Locate platelets.
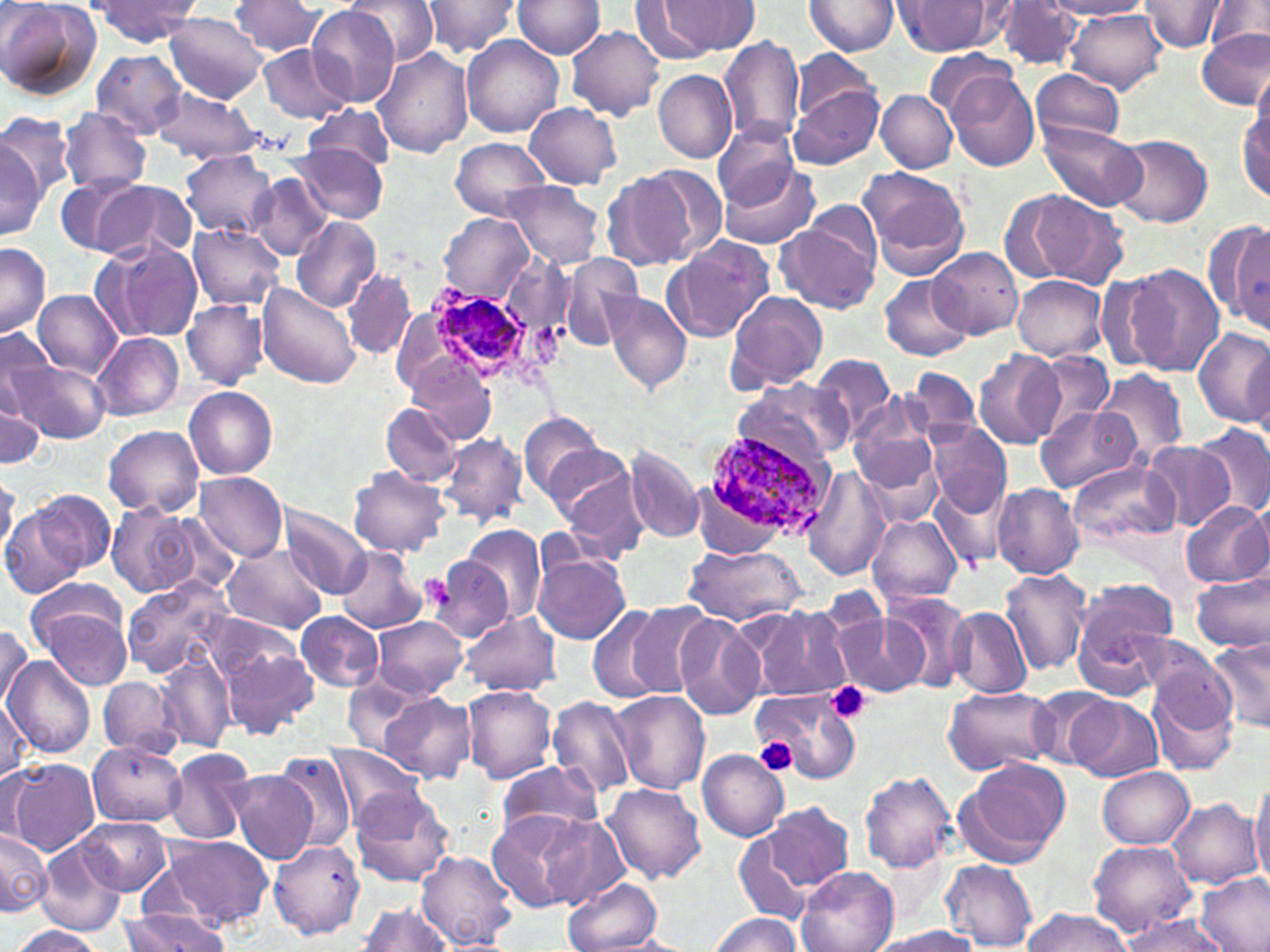
Approximate bounding boxes as named x1/y1/x2/y2 corners in pixels.
Platelets: (x1=826, y1=681, x2=872, y2=724), (x1=750, y1=737, x2=799, y2=777).

slide-level diagnosis = Plasmodium ovale
modality = optical microscopy
magnification = 1000x
field of view = single
preparation = thin blood smear
image size = 1270×952 pixels
uninfected red blood cell locations = approximate bounding boxes as named x1/y1/x2/y2 corners in pixels: (x1=346, y1=0, x2=438, y2=65), (x1=511, y1=0, x2=605, y2=59), (x1=1204, y1=0, x2=1268, y2=55), (x1=0, y1=1, x2=100, y2=102), (x1=231, y1=1, x2=323, y2=56), (x1=420, y1=1, x2=521, y2=59), (x1=668, y1=1, x2=761, y2=55), (x1=803, y1=1, x2=899, y2=57), (x1=999, y1=1, x2=1083, y2=71), (x1=1047, y1=1, x2=1152, y2=19), (x1=89, y1=2, x2=199, y2=47), (x1=629, y1=2, x2=721, y2=63), (x1=895, y1=2, x2=999, y2=57), (x1=1138, y1=2, x2=1224, y2=53), (x1=307, y1=6, x2=400, y2=107), (x1=1066, y1=8, x2=1169, y2=92), (x1=165, y1=13, x2=266, y2=103), (x1=564, y1=25, x2=663, y2=120), (x1=1197, y1=27, x2=1270, y2=110), (x1=718, y1=34, x2=806, y2=146), (x1=461, y1=35, x2=564, y2=138), (x1=258, y1=44, x2=352, y2=121), (x1=373, y1=48, x2=474, y2=158), (x1=793, y1=48, x2=879, y2=125), (x1=926, y1=48, x2=1018, y2=123), (x1=90, y1=49, x2=189, y2=139), (x1=1032, y1=69, x2=1126, y2=148), (x1=1248, y1=69, x2=1270, y2=164), (x1=653, y1=70, x2=737, y2=164), (x1=946, y1=71, x2=1040, y2=172), (x1=789, y1=86, x2=882, y2=168), (x1=151, y1=88, x2=267, y2=165), (x1=875, y1=90, x2=957, y2=173), (x1=525, y1=102, x2=621, y2=189), (x1=303, y1=103, x2=395, y2=171), (x1=1237, y1=106, x2=1269, y2=201), (x1=57, y1=109, x2=151, y2=194), (x1=0, y1=113, x2=77, y2=208), (x1=1038, y1=121, x2=1144, y2=212), (x1=713, y1=122, x2=801, y2=209), (x1=0, y1=133, x2=46, y2=237), (x1=1111, y1=134, x2=1214, y2=228), (x1=450, y1=138, x2=550, y2=221), (x1=294, y1=145, x2=387, y2=223), (x1=179, y1=150, x2=279, y2=240), (x1=718, y1=159, x2=820, y2=250), (x1=633, y1=166, x2=724, y2=264), (x1=858, y1=166, x2=970, y2=277), (x1=603, y1=169, x2=691, y2=271), (x1=57, y1=174, x2=146, y2=259), (x1=248, y1=174, x2=333, y2=260), (x1=95, y1=180, x2=196, y2=261), (x1=500, y1=180, x2=606, y2=271), (x1=1007, y1=189, x2=1129, y2=289), (x1=439, y1=212, x2=532, y2=303), (x1=289, y1=215, x2=381, y2=312), (x1=775, y1=218, x2=880, y2=315), (x1=187, y1=224, x2=284, y2=310), (x1=1222, y1=224, x2=1269, y2=336), (x1=661, y1=238, x2=773, y2=344), (x1=105, y1=240, x2=204, y2=342), (x1=0, y1=244, x2=51, y2=338), (x1=931, y1=248, x2=1022, y2=338), (x1=500, y1=251, x2=576, y2=342), (x1=558, y1=254, x2=643, y2=350), (x1=1118, y1=264, x2=1224, y2=374), (x1=343, y1=267, x2=416, y2=360), (x1=877, y1=273, x2=971, y2=361), (x1=1012, y1=275, x2=1108, y2=361), (x1=258, y1=284, x2=361, y2=391), (x1=33, y1=290, x2=122, y2=379), (x1=723, y1=290, x2=829, y2=395), (x1=601, y1=292, x2=692, y2=394), (x1=183, y1=299, x2=268, y2=389), (x1=1192, y1=326, x2=1270, y2=426), (x1=0, y1=327, x2=58, y2=422), (x1=91, y1=332, x2=183, y2=420), (x1=974, y1=350, x2=1063, y2=451), (x1=1029, y1=351, x2=1116, y2=439), (x1=808, y1=354, x2=898, y2=448), (x1=410, y1=357, x2=499, y2=443), (x1=12, y1=359, x2=110, y2=444), (x1=1092, y1=367, x2=1190, y2=463), (x1=905, y1=368, x2=982, y2=445), (x1=733, y1=379, x2=850, y2=469), (x1=0, y1=383, x2=45, y2=470), (x1=185, y1=387, x2=277, y2=480), (x1=380, y1=401, x2=462, y2=487), (x1=1035, y1=405, x2=1142, y2=494), (x1=518, y1=411, x2=607, y2=501), (x1=850, y1=412, x2=941, y2=493), (x1=927, y1=421, x2=1012, y2=514), (x1=103, y1=424, x2=204, y2=517), (x1=1193, y1=424, x2=1270, y2=521), (x1=438, y1=433, x2=529, y2=530), (x1=1141, y1=439, x2=1233, y2=530), (x1=855, y1=441, x2=944, y2=531), (x1=543, y1=442, x2=642, y2=537), (x1=624, y1=446, x2=705, y2=545), (x1=1066, y1=459, x2=1180, y2=548), (x1=348, y1=466, x2=450, y2=557), (x1=560, y1=469, x2=653, y2=564), (x1=195, y1=472, x2=288, y2=560), (x1=0, y1=474, x2=19, y2=557), (x1=929, y1=477, x2=1011, y2=569), (x1=992, y1=483, x2=1085, y2=578), (x1=30, y1=488, x2=117, y2=576), (x1=1177, y1=500, x2=1270, y2=589), (x1=1, y1=501, x2=93, y2=600), (x1=107, y1=501, x2=202, y2=597), (x1=1236, y1=501, x2=1270, y2=583), (x1=280, y1=502, x2=374, y2=598), (x1=866, y1=513, x2=962, y2=609), (x1=463, y1=525, x2=545, y2=625), (x1=221, y1=543, x2=327, y2=635), (x1=684, y1=543, x2=804, y2=627), (x1=336, y1=546, x2=427, y2=634), (x1=424, y1=554, x2=516, y2=645), (x1=533, y1=554, x2=631, y2=644), (x1=999, y1=568, x2=1095, y2=675), (x1=1192, y1=572, x2=1270, y2=652), (x1=120, y1=576, x2=236, y2=679), (x1=1070, y1=588, x2=1177, y2=699), (x1=31, y1=590, x2=134, y2=689), (x1=882, y1=592, x2=975, y2=693), (x1=621, y1=601, x2=719, y2=694), (x1=585, y1=605, x2=671, y2=705), (x1=747, y1=605, x2=852, y2=702), (x1=946, y1=608, x2=1031, y2=699), (x1=295, y1=611, x2=384, y2=691), (x1=462, y1=611, x2=561, y2=697), (x1=673, y1=612, x2=763, y2=721), (x1=836, y1=614, x2=926, y2=698), (x1=372, y1=615, x2=468, y2=698), (x1=0, y1=624, x2=32, y2=710), (x1=218, y1=635, x2=316, y2=738), (x1=1142, y1=637, x2=1240, y2=737), (x1=1208, y1=638, x2=1270, y2=734), (x1=154, y1=655, x2=236, y2=754), (x1=4, y1=657, x2=96, y2=757), (x1=341, y1=673, x2=430, y2=756), (x1=98, y1=676, x2=185, y2=759), (x1=460, y1=684, x2=558, y2=784), (x1=1147, y1=685, x2=1237, y2=778), (x1=944, y1=686, x2=1055, y2=774), (x1=1027, y1=688, x2=1116, y2=769), (x1=757, y1=689, x2=862, y2=786), (x1=610, y1=690, x2=710, y2=794), (x1=0, y1=692, x2=35, y2=784), (x1=377, y1=693, x2=477, y2=784), (x1=547, y1=695, x2=637, y2=798), (x1=1069, y1=697, x2=1162, y2=783), (x1=87, y1=741, x2=186, y2=827), (x1=327, y1=745, x2=422, y2=825), (x1=164, y1=748, x2=257, y2=844), (x1=268, y1=750, x2=358, y2=853), (x1=697, y1=750, x2=789, y2=841), (x1=7, y1=757, x2=101, y2=856), (x1=957, y1=757, x2=1072, y2=864), (x1=496, y1=761, x2=602, y2=841), (x1=1099, y1=765, x2=1196, y2=848), (x1=232, y1=770, x2=318, y2=863), (x1=860, y1=772, x2=958, y2=873), (x1=1248, y1=778, x2=1270, y2=888), (x1=351, y1=783, x2=455, y2=889), (x1=603, y1=783, x2=707, y2=883), (x1=1168, y1=798, x2=1261, y2=889), (x1=761, y1=801, x2=854, y2=894), (x1=486, y1=811, x2=591, y2=912), (x1=540, y1=814, x2=631, y2=912), (x1=76, y1=816, x2=172, y2=895), (x1=732, y1=825, x2=826, y2=928), (x1=1, y1=828, x2=51, y2=917), (x1=161, y1=835, x2=273, y2=928), (x1=36, y1=837, x2=126, y2=937), (x1=268, y1=840, x2=365, y2=940), (x1=1088, y1=840, x2=1197, y2=935), (x1=417, y1=850, x2=518, y2=951), (x1=942, y1=860, x2=1038, y2=950), (x1=797, y1=865, x2=898, y2=952), (x1=1198, y1=872, x2=1270, y2=952), (x1=562, y1=876, x2=663, y2=952), (x1=357, y1=902, x2=455, y2=951), (x1=1019, y1=908, x2=1132, y2=952), (x1=120, y1=909, x2=230, y2=951), (x1=707, y1=914, x2=803, y2=952), (x1=1117, y1=915, x2=1228, y2=952), (x1=868, y1=924, x2=985, y2=951), (x1=9, y1=926, x2=106, y2=951)
stain = May-Grünwald-Giemsa